Identify the blood parasite species.
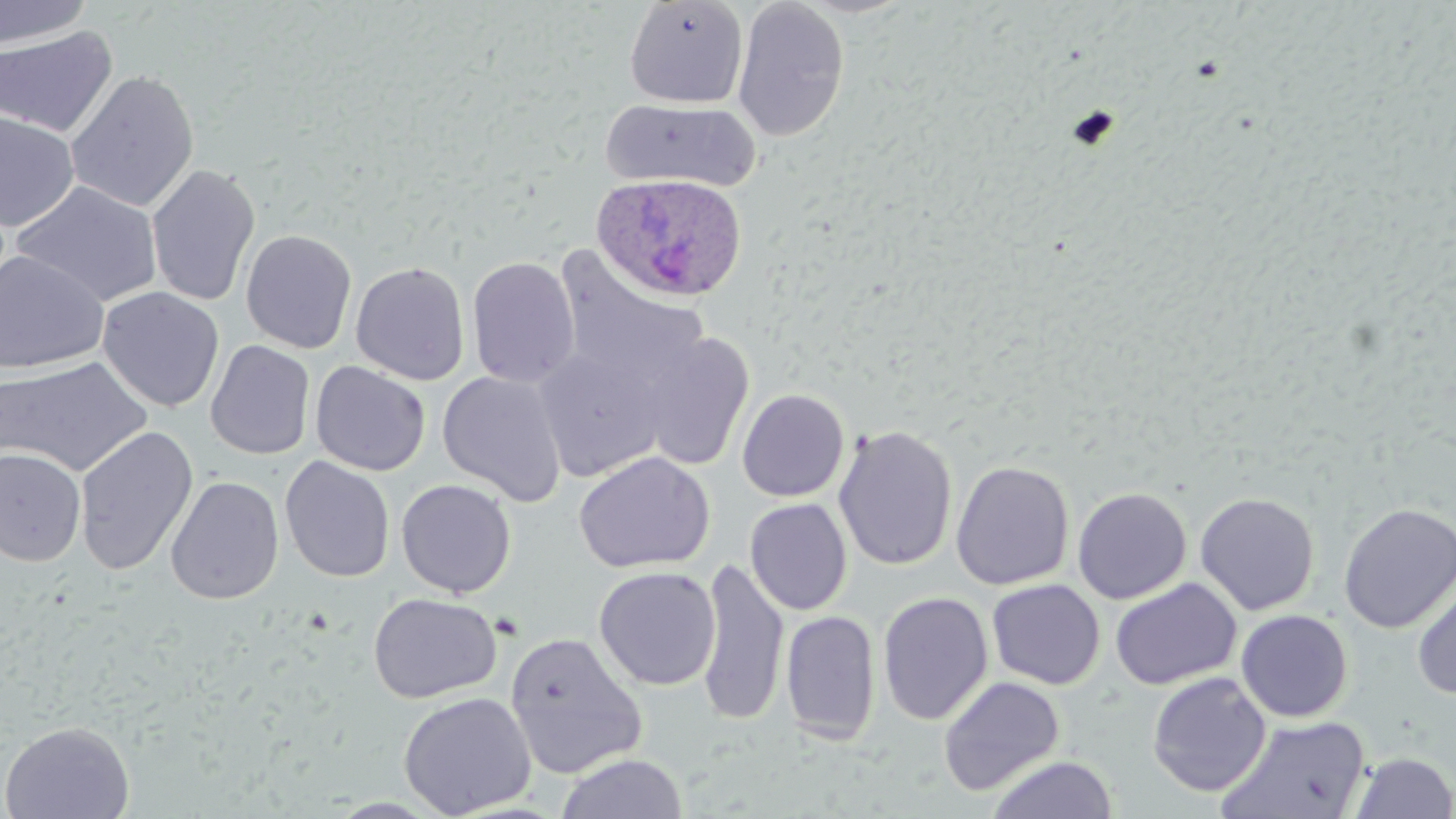

Plasmodium ovale.

Approximate bounding boxes as named x1/y1/x2/y2 corners in pixels. Plasmodium ovale-infected red blood cell locations: (x1=591, y1=175, x2=746, y2=305). Uninfected red blood cell locations: (x1=0, y1=0, x2=95, y2=49), (x1=623, y1=0, x2=749, y2=109), (x1=731, y1=0, x2=850, y2=143), (x1=0, y1=25, x2=117, y2=139), (x1=65, y1=69, x2=200, y2=213), (x1=600, y1=98, x2=761, y2=194), (x1=0, y1=111, x2=80, y2=231), (x1=146, y1=163, x2=261, y2=308), (x1=10, y1=180, x2=164, y2=308), (x1=240, y1=229, x2=358, y2=354), (x1=552, y1=250, x2=712, y2=400), (x1=0, y1=251, x2=109, y2=374), (x1=466, y1=256, x2=580, y2=389), (x1=350, y1=261, x2=471, y2=385), (x1=97, y1=287, x2=225, y2=412), (x1=635, y1=331, x2=753, y2=472), (x1=205, y1=339, x2=316, y2=460), (x1=534, y1=344, x2=668, y2=481), (x1=0, y1=356, x2=153, y2=478), (x1=309, y1=361, x2=432, y2=476), (x1=438, y1=371, x2=567, y2=507), (x1=737, y1=388, x2=850, y2=502), (x1=832, y1=423, x2=958, y2=572), (x1=74, y1=425, x2=198, y2=576), (x1=0, y1=447, x2=86, y2=566), (x1=574, y1=451, x2=714, y2=574), (x1=279, y1=456, x2=395, y2=583), (x1=951, y1=460, x2=1075, y2=590), (x1=280, y1=469, x2=515, y2=588), (x1=165, y1=475, x2=284, y2=605), (x1=396, y1=479, x2=517, y2=598), (x1=1072, y1=486, x2=1192, y2=604), (x1=1194, y1=491, x2=1320, y2=616), (x1=745, y1=498, x2=852, y2=615), (x1=1338, y1=502, x2=1456, y2=633), (x1=696, y1=558, x2=789, y2=726), (x1=593, y1=566, x2=721, y2=691), (x1=1411, y1=572, x2=1456, y2=700), (x1=1110, y1=577, x2=1242, y2=691), (x1=986, y1=579, x2=1105, y2=690), (x1=876, y1=591, x2=993, y2=726), (x1=368, y1=592, x2=502, y2=704), (x1=1235, y1=609, x2=1353, y2=722), (x1=780, y1=610, x2=881, y2=745), (x1=505, y1=631, x2=648, y2=779), (x1=1147, y1=672, x2=1271, y2=797), (x1=938, y1=676, x2=1065, y2=797), (x1=398, y1=691, x2=537, y2=818), (x1=1217, y1=715, x2=1372, y2=819), (x1=0, y1=721, x2=135, y2=819), (x1=1349, y1=751, x2=1456, y2=818), (x1=555, y1=752, x2=689, y2=818), (x1=986, y1=755, x2=1117, y2=818). Single field of view. Thin blood smear. May-Grünwald-Giemsa stain. Image is 1456×819 pixels. 1000x magnification. Light microscopy.